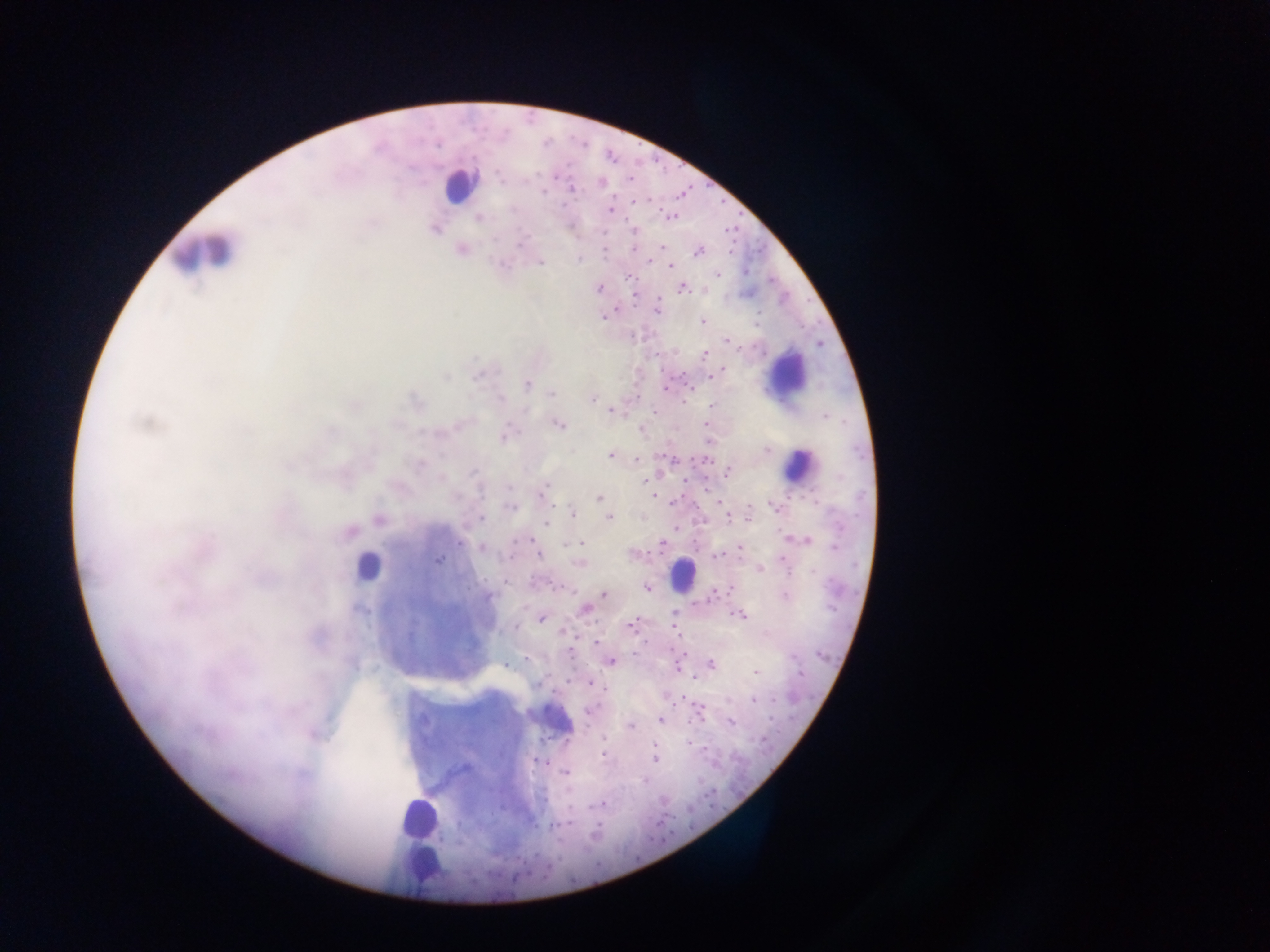

Approximate centers as x y in pixels.
Summary:
  - Leukocyte locations: 459 185; 204 253; 785 373; 798 466; 368 567; 681 574; 554 719; 418 819; 422 866
  - Malaria parasite locations: 631 179; 600 182; 570 189; 610 210; 670 216; 478 217; 434 228; 635 231; 661 247; 462 248; 605 251; 698 251; 579 259; 540 262; 649 262; 503 263; 670 265; 718 274; 630 278; 599 288; 682 288; 635 294; 615 310; 657 310; 701 322; 727 341; 704 355; 725 369; 710 375; 528 385; 665 389; 552 393; 592 397; 606 406; 610 410; 654 412; 145 423; 558 424; 706 425; 640 429; 504 434; 766 450; 610 454; 636 459; 704 459; 729 470; 646 478; 542 493; 654 496; 599 497; 673 502; 719 503; 510 506; 775 507; 573 514; 749 517; 379 518; 480 518; 608 518; 727 518; 546 522; 676 528; 348 532; 805 540; 582 543; 661 545; 481 547; 740 547; 538 554; 715 554; 783 558; 438 560; 579 563; 759 568; 505 581; 647 587; 729 589; 603 594; 785 595; 584 608; 739 614; 541 617; 631 626; 515 627; 595 643; 679 657; 609 661; 710 664; 677 666; 756 671; 695 678; 536 684; 590 684; 603 687; 754 700; 699 712; 661 719; 730 722; 630 725; 313 733; 686 741; 655 742; 604 754; 655 758; 543 762; 566 772; 645 780; 603 804; 568 822
  - Field of view: single
  - Country: Ghana
  - Image size: 1270×952 pixels
  - Preparation: thick blood film
  - Capture: mobile-phone photograph through a microscope